Report the malaria status of this cell.
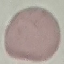
Uninfected.

image type = cell patch, automatically extracted from a larger field of view and resized to 64 × 64 pixels
capture = smartphone camera at the microscope eyepiece
preparation = thin blood film
stain = Giemsa